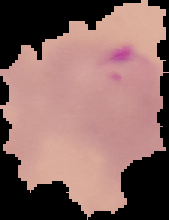
Summary:
  - Result: malaria parasites identified
  - Preparation: thin blood smear
  - Image type: segmented cell region on a black background
  - Image size: 169×220 pixels